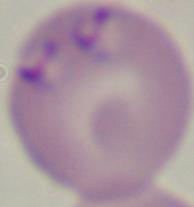

Summary:
  - Identification: Babesia
  - Modality: photomicrograph
  - Magnification: 1000x